Describe the morphology of the erythrocytes.
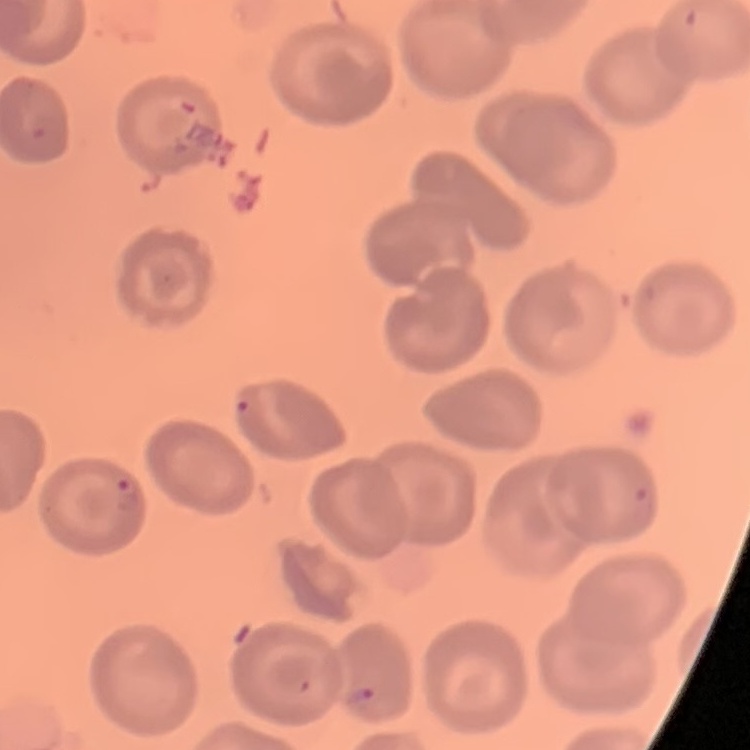

No rouleaux formation.

Summary:
  - Image type: square crop of a larger photomicrograph
  - Stain: Field's or Giemsa
  - Preparation: thin blood film